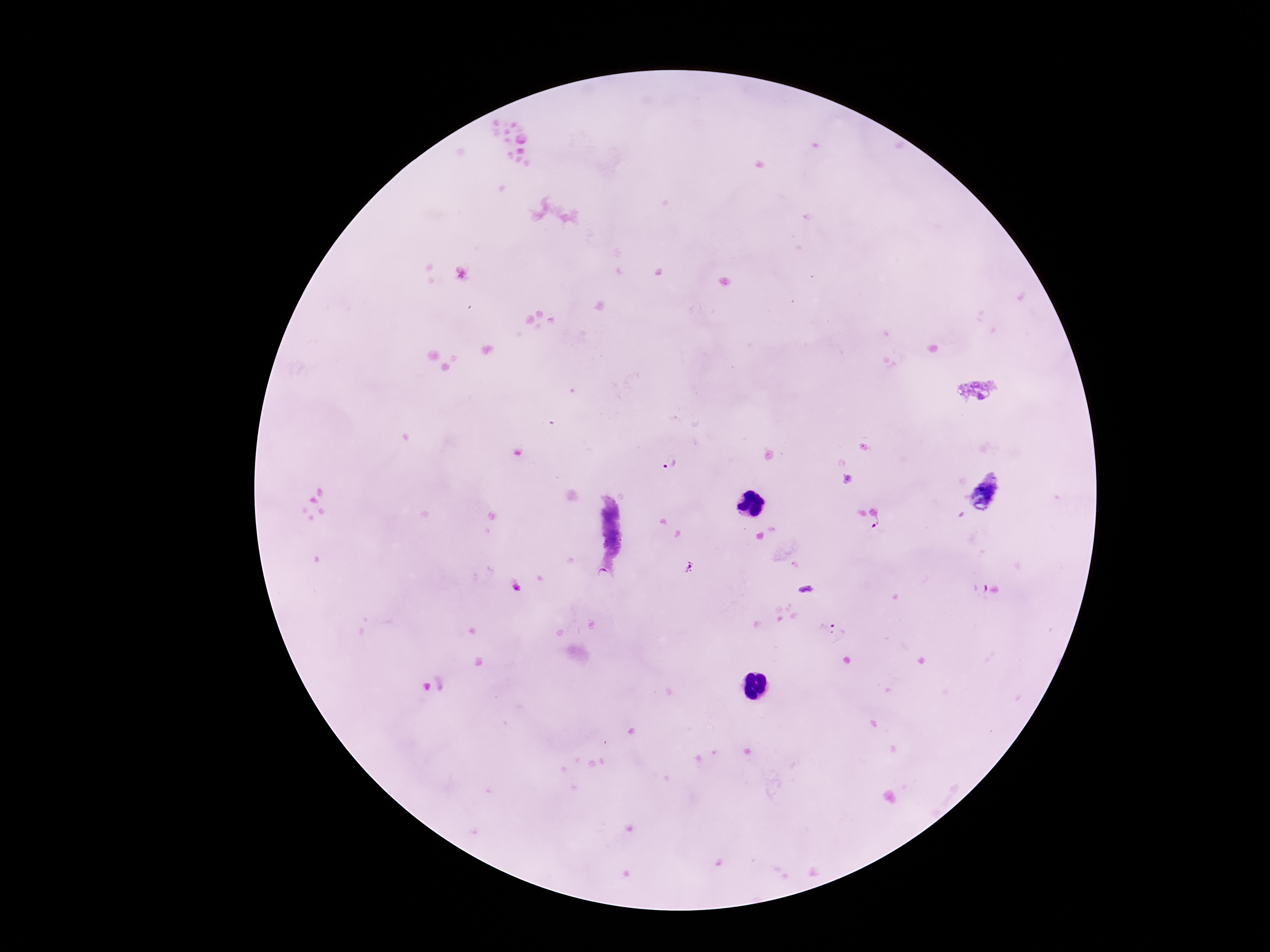
preparation = thick blood smear
capture = smartphone camera through the microscope eyepiece
Plasmodium parasite locations = approximate object centers, in pixels from the top-left corner: (x=670, y=463), (x=988, y=492), (x=878, y=523), (x=689, y=568), (x=832, y=630)
magnification = 100x
image size = 1270×952 pixels
field of view = one from this slide
patient malaria status = positive
stain = Giemsa